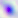

magnification = 400x
modality = photomicrograph
identification = Toxoplasma gondii